Report the malaria status of this cell.
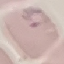

Parasitized.

Photographed with a smartphone camera at the microscope eyepiece. Giemsa stain. Automatically extracted cell patch, resized to 64 × 64 pixels. Thin blood smear.